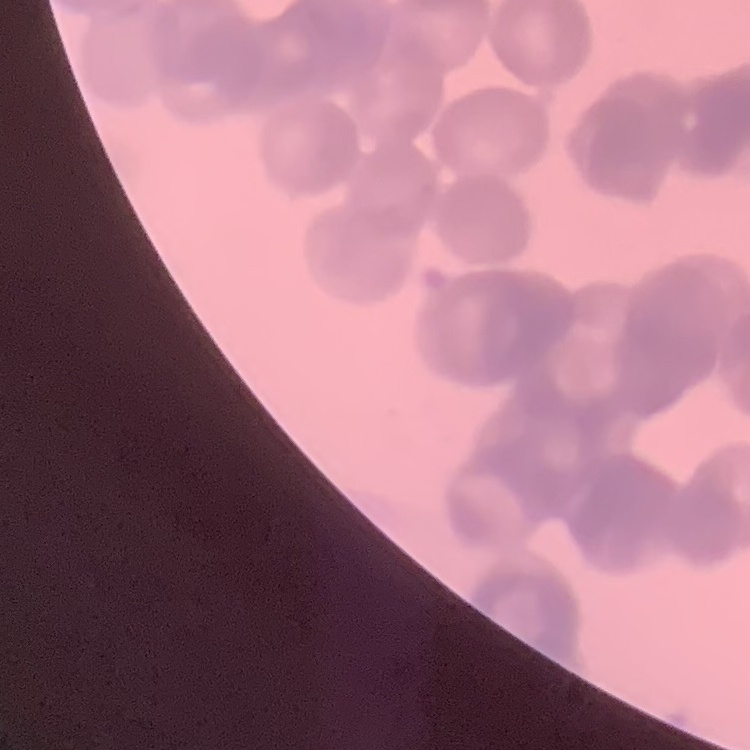
Summary:
  - Red blood cell morphology: rouleaux formation
  - Preparation: thin blood film
  - Stain: Field's or Giemsa
  - Image type: one tile cut from a larger photomicrograph